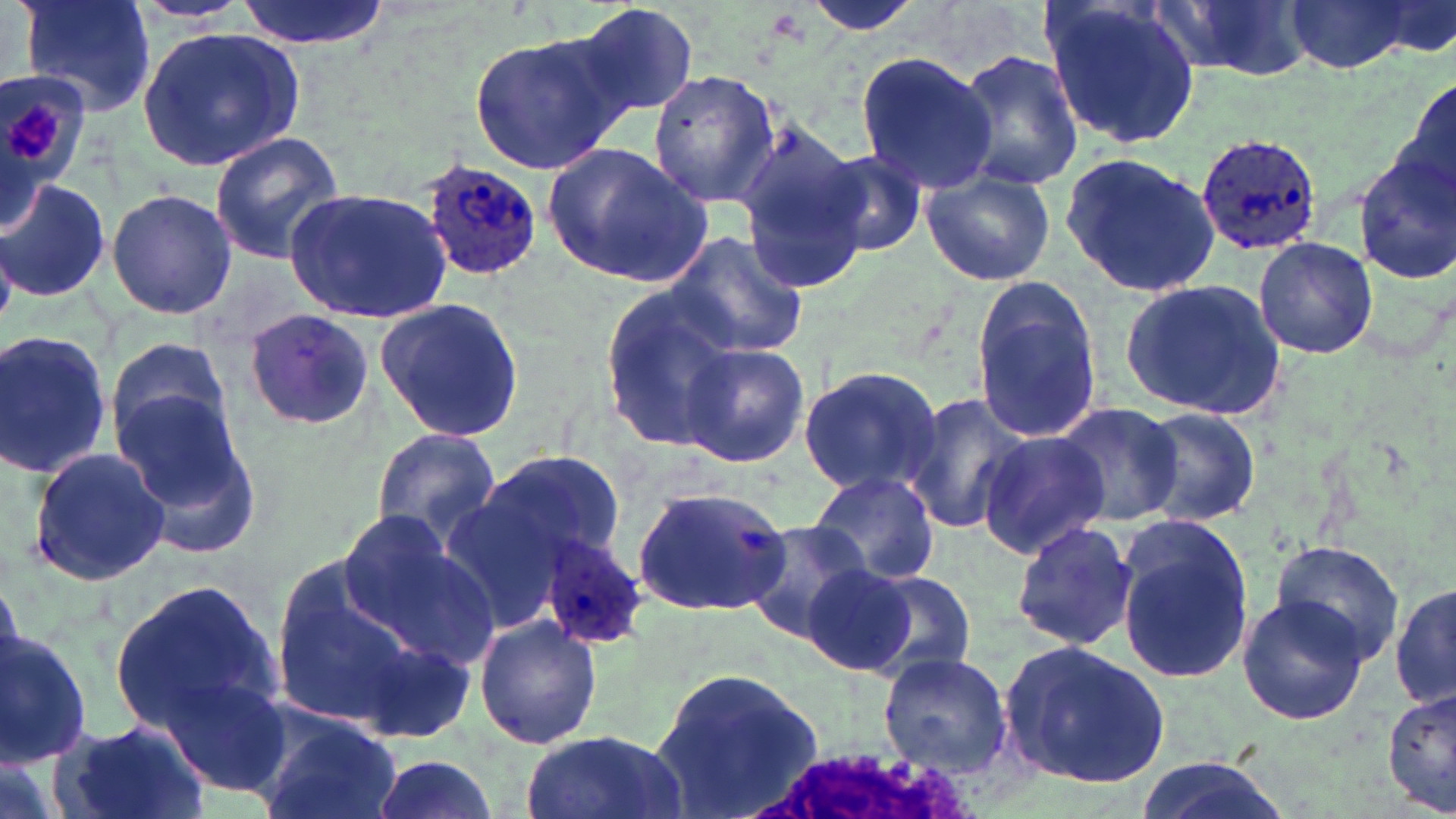
Summary:
  - Coordinate format: approximate bounding boxes as [x1, y1, x2, y2] in pixels
  - Plasmodium ovale-infected red blood cell locations: [1194, 135, 1325, 255], [421, 158, 544, 283], [539, 535, 650, 650]
  - Uninfected red blood cell locations: [19, 0, 157, 118], [236, 0, 390, 50], [1156, 0, 1316, 81], [793, 1, 933, 36], [1043, 1, 1204, 149], [1282, 1, 1423, 74], [574, 2, 701, 123], [140, 25, 303, 172], [468, 31, 626, 175], [948, 48, 1084, 190], [853, 51, 996, 196], [0, 68, 93, 209], [649, 69, 782, 209], [1397, 71, 1456, 211], [735, 125, 875, 293], [209, 132, 346, 263], [541, 142, 711, 286], [818, 147, 929, 259], [1060, 151, 1219, 296], [1351, 151, 1456, 284], [919, 165, 1056, 287], [0, 176, 110, 304], [285, 187, 449, 323], [106, 188, 236, 320], [663, 230, 809, 360], [1252, 238, 1378, 359], [1123, 277, 1286, 421], [971, 279, 1102, 441], [598, 284, 746, 452], [374, 297, 525, 440], [243, 309, 374, 430], [0, 330, 113, 479], [106, 334, 234, 461], [676, 342, 811, 467], [798, 364, 943, 500], [114, 389, 261, 557], [905, 392, 1031, 537], [1051, 401, 1183, 528], [1132, 405, 1261, 526], [369, 428, 504, 550], [976, 429, 1108, 559], [27, 447, 170, 585], [476, 448, 626, 575], [808, 470, 939, 588], [632, 483, 793, 619], [335, 509, 498, 673], [743, 518, 879, 646], [1010, 521, 1139, 651], [1113, 522, 1252, 686], [1270, 538, 1407, 669], [261, 551, 478, 745], [802, 564, 918, 674], [857, 569, 977, 682], [110, 579, 278, 737], [1390, 581, 1454, 713], [1236, 595, 1372, 723], [474, 615, 602, 750], [0, 629, 91, 764], [997, 641, 1172, 790], [877, 651, 1013, 778], [648, 663, 826, 817], [156, 669, 291, 798], [1381, 687, 1456, 816], [251, 708, 403, 819], [53, 720, 208, 819], [517, 730, 685, 819], [365, 752, 502, 819], [1127, 757, 1304, 819]
  - Platelet locations: [7, 102, 61, 162]
  - Slide-level diagnosis: Plasmodium ovale
  - Field of view: single
  - Magnification: 1000x
  - Preparation: thin blood film
  - Stain: May-Grünwald-Giemsa
  - Image size: 1456×819 pixels
  - Modality: light microscopy